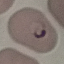
Result: malaria parasites detected. Automatically extracted cell patch, resized to 64 × 64 pixels. Thin blood film. Photographed with a smartphone camera at the microscope eyepiece. Giemsa-stained preparation.